Identify the parasite.
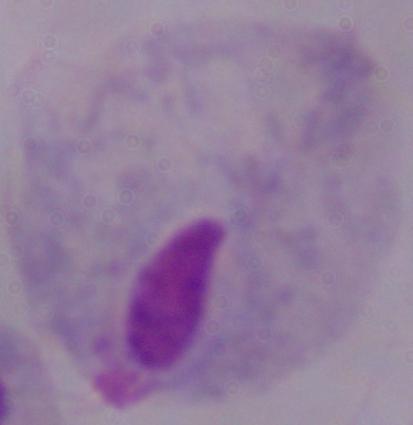
A trichomonad.

modality = micrograph
magnification = 1000x